Give the extent of all Plasmodium vivax-infected red blood cells.
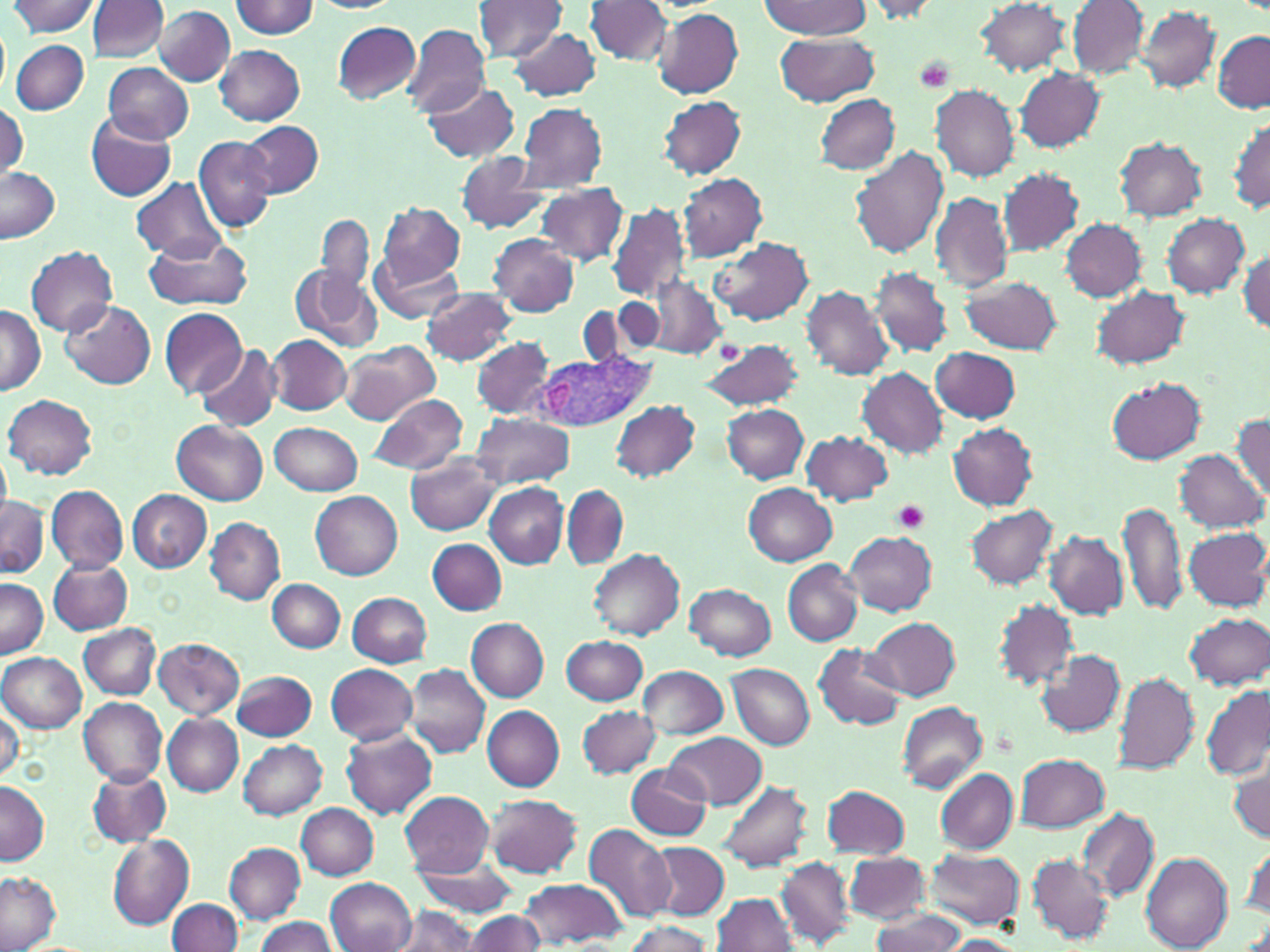
Approximate bounding boxes as named x1/y1/x2/y2 corners in pixels.
Plasmodium vivax-infected red blood cells: (x1=535, y1=352, x2=653, y2=434).

Uninfected red blood cell locations: (x1=231, y1=0, x2=318, y2=38), (x1=471, y1=0, x2=567, y2=63), (x1=760, y1=0, x2=869, y2=38), (x1=974, y1=0, x2=1071, y2=76), (x1=8, y1=1, x2=101, y2=37), (x1=86, y1=1, x2=167, y2=62), (x1=584, y1=1, x2=673, y2=67), (x1=857, y1=1, x2=942, y2=22), (x1=1067, y1=1, x2=1149, y2=78), (x1=154, y1=6, x2=235, y2=85), (x1=1138, y1=6, x2=1220, y2=93), (x1=651, y1=7, x2=743, y2=98), (x1=332, y1=21, x2=420, y2=103), (x1=400, y1=25, x2=490, y2=119), (x1=507, y1=27, x2=602, y2=102), (x1=1212, y1=30, x2=1269, y2=113), (x1=773, y1=33, x2=879, y2=106), (x1=12, y1=39, x2=88, y2=115), (x1=215, y1=44, x2=306, y2=126), (x1=103, y1=63, x2=194, y2=143), (x1=1014, y1=67, x2=1103, y2=152), (x1=421, y1=81, x2=519, y2=162), (x1=931, y1=84, x2=1021, y2=181), (x1=813, y1=93, x2=901, y2=174), (x1=658, y1=94, x2=747, y2=180), (x1=0, y1=101, x2=28, y2=180), (x1=515, y1=101, x2=606, y2=193), (x1=87, y1=114, x2=178, y2=203), (x1=1228, y1=119, x2=1269, y2=213), (x1=239, y1=121, x2=323, y2=197), (x1=193, y1=135, x2=277, y2=233), (x1=1114, y1=137, x2=1207, y2=221), (x1=849, y1=146, x2=949, y2=259), (x1=455, y1=152, x2=552, y2=233), (x1=0, y1=166, x2=61, y2=243), (x1=997, y1=168, x2=1084, y2=256), (x1=863, y1=169, x2=1009, y2=280), (x1=678, y1=173, x2=768, y2=262), (x1=130, y1=178, x2=225, y2=261), (x1=534, y1=184, x2=630, y2=266), (x1=930, y1=192, x2=1014, y2=294), (x1=377, y1=202, x2=466, y2=288), (x1=608, y1=202, x2=691, y2=304), (x1=1162, y1=214, x2=1251, y2=298), (x1=317, y1=216, x2=374, y2=296), (x1=1060, y1=218, x2=1147, y2=302), (x1=145, y1=233, x2=254, y2=313), (x1=489, y1=235, x2=577, y2=315), (x1=711, y1=237, x2=814, y2=326), (x1=25, y1=245, x2=118, y2=335), (x1=1237, y1=248, x2=1270, y2=336), (x1=370, y1=252, x2=462, y2=324), (x1=291, y1=262, x2=383, y2=351), (x1=869, y1=266, x2=953, y2=357), (x1=639, y1=277, x2=727, y2=360), (x1=962, y1=277, x2=1061, y2=353), (x1=801, y1=284, x2=897, y2=382), (x1=1092, y1=285, x2=1192, y2=370), (x1=422, y1=287, x2=517, y2=365), (x1=606, y1=298, x2=665, y2=357), (x1=59, y1=299, x2=156, y2=390), (x1=0, y1=305, x2=45, y2=395), (x1=160, y1=308, x2=248, y2=399), (x1=267, y1=335, x2=352, y2=416), (x1=472, y1=336, x2=556, y2=418), (x1=697, y1=339, x2=805, y2=411), (x1=339, y1=341, x2=440, y2=424), (x1=195, y1=344, x2=280, y2=431), (x1=931, y1=346, x2=1022, y2=424), (x1=856, y1=367, x2=948, y2=460), (x1=1105, y1=376, x2=1206, y2=463), (x1=368, y1=393, x2=468, y2=476), (x1=3, y1=395, x2=97, y2=479), (x1=612, y1=400, x2=701, y2=483), (x1=722, y1=404, x2=809, y2=483), (x1=1231, y1=412, x2=1269, y2=502), (x1=471, y1=413, x2=574, y2=488), (x1=173, y1=420, x2=268, y2=505), (x1=270, y1=421, x2=363, y2=497), (x1=947, y1=423, x2=1037, y2=510), (x1=801, y1=431, x2=893, y2=506), (x1=1176, y1=449, x2=1266, y2=533), (x1=407, y1=453, x2=502, y2=534), (x1=743, y1=482, x2=837, y2=563), (x1=485, y1=483, x2=568, y2=568), (x1=46, y1=485, x2=129, y2=574), (x1=563, y1=486, x2=628, y2=568), (x1=128, y1=490, x2=211, y2=572), (x1=310, y1=490, x2=403, y2=580), (x1=0, y1=493, x2=48, y2=577), (x1=1119, y1=500, x2=1189, y2=618), (x1=966, y1=504, x2=1060, y2=590), (x1=205, y1=517, x2=284, y2=604), (x1=1184, y1=526, x2=1270, y2=611), (x1=844, y1=530, x2=937, y2=615), (x1=1045, y1=532, x2=1128, y2=619), (x1=428, y1=538, x2=507, y2=615), (x1=588, y1=550, x2=685, y2=641), (x1=783, y1=558, x2=864, y2=645), (x1=49, y1=559, x2=132, y2=634), (x1=0, y1=577, x2=47, y2=658), (x1=268, y1=579, x2=345, y2=653), (x1=685, y1=582, x2=777, y2=661), (x1=347, y1=592, x2=431, y2=667), (x1=994, y1=600, x2=1078, y2=691), (x1=1184, y1=612, x2=1269, y2=689), (x1=866, y1=616, x2=961, y2=700), (x1=466, y1=619, x2=548, y2=701), (x1=79, y1=623, x2=161, y2=700), (x1=561, y1=636, x2=647, y2=704), (x1=153, y1=637, x2=245, y2=718), (x1=813, y1=643, x2=907, y2=732), (x1=1035, y1=649, x2=1126, y2=738), (x1=0, y1=652, x2=85, y2=731), (x1=404, y1=663, x2=491, y2=757), (x1=326, y1=664, x2=419, y2=745), (x1=727, y1=664, x2=813, y2=748), (x1=637, y1=665, x2=729, y2=739), (x1=233, y1=669, x2=317, y2=741), (x1=1113, y1=673, x2=1200, y2=773), (x1=1202, y1=684, x2=1269, y2=781), (x1=79, y1=697, x2=167, y2=785), (x1=898, y1=700, x2=987, y2=792), (x1=0, y1=704, x2=23, y2=783), (x1=481, y1=705, x2=565, y2=791), (x1=577, y1=705, x2=660, y2=778), (x1=162, y1=714, x2=244, y2=795), (x1=341, y1=728, x2=439, y2=818), (x1=665, y1=732, x2=766, y2=808), (x1=238, y1=740, x2=327, y2=819), (x1=1015, y1=754, x2=1109, y2=832), (x1=1230, y1=759, x2=1270, y2=844), (x1=627, y1=763, x2=714, y2=840), (x1=935, y1=767, x2=1019, y2=853), (x1=88, y1=768, x2=173, y2=848), (x1=0, y1=779, x2=49, y2=865), (x1=719, y1=780, x2=814, y2=873), (x1=820, y1=785, x2=910, y2=860), (x1=398, y1=791, x2=494, y2=877), (x1=486, y1=793, x2=580, y2=876), (x1=297, y1=803, x2=380, y2=878), (x1=1076, y1=808, x2=1160, y2=902), (x1=584, y1=824, x2=674, y2=924), (x1=108, y1=835, x2=194, y2=929), (x1=1244, y1=839, x2=1270, y2=925), (x1=645, y1=841, x2=730, y2=920), (x1=225, y1=843, x2=305, y2=924), (x1=924, y1=848, x2=1024, y2=928), (x1=1140, y1=851, x2=1232, y2=950), (x1=844, y1=852, x2=929, y2=924), (x1=1027, y1=854, x2=1114, y2=944), (x1=410, y1=856, x2=519, y2=915), (x1=776, y1=858, x2=853, y2=947), (x1=0, y1=870, x2=61, y2=952), (x1=517, y1=876, x2=626, y2=947), (x1=327, y1=878, x2=416, y2=952), (x1=713, y1=892, x2=799, y2=951), (x1=167, y1=898, x2=243, y2=952), (x1=388, y1=905, x2=481, y2=952), (x1=867, y1=908, x2=969, y2=952), (x1=461, y1=910, x2=547, y2=952), (x1=252, y1=916, x2=339, y2=952), (x1=619, y1=921, x2=717, y2=952), (x1=938, y1=935, x2=1026, y2=951). Platelet locations: (x1=913, y1=56, x2=956, y2=96), (x1=893, y1=500, x2=929, y2=532). Slide-level diagnosis: Plasmodium vivax. Thin blood smear. May-Grünwald-Giemsa stain. One field of a larger specimen. 1000x magnification. Light microscopy. Image is 1270×952 pixels.